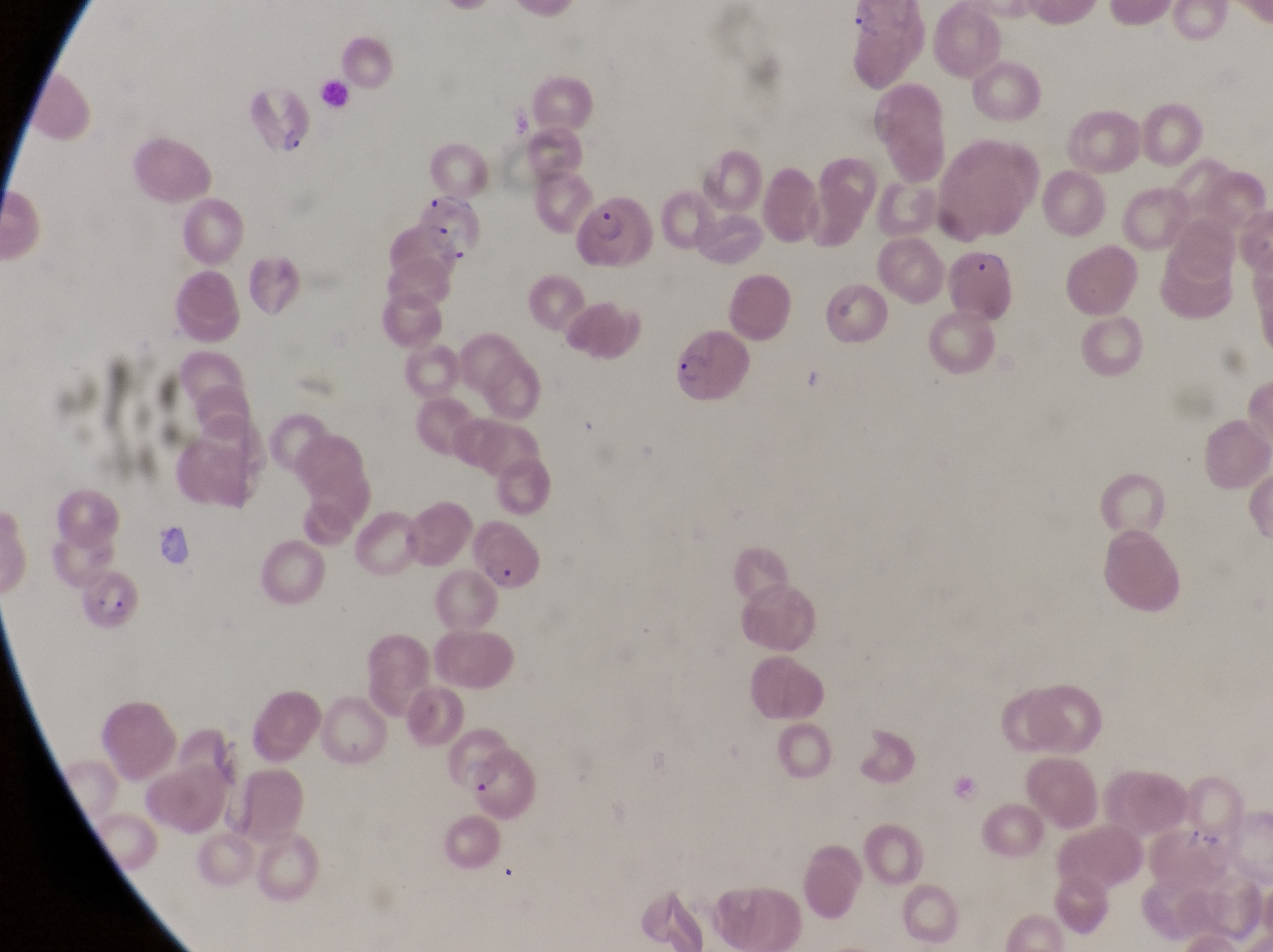

Approximate bounding boxes as (left, top, right, bottom) in pixels.
Summary:
  - Parasitised red blood cell locations: (840, 5, 918, 79), (244, 80, 316, 160), (412, 183, 487, 270), (574, 188, 657, 276), (941, 235, 1015, 322), (671, 329, 756, 414), (474, 537, 548, 599), (82, 570, 149, 633), (443, 732, 514, 792)
  - Leukocyte locations: (322, 81, 360, 117)
  - Magnification: 1000x
  - Country: Uganda
  - Capture: smartphone photograph through the eyepiece of an Olympus CX-23 microscope
  - Image size: 1273×952 pixels
  - Preparation: thin blood smear
  - Field of view: single